Classify this cell by malaria status.
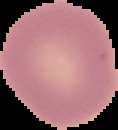

Uninfected.

image size = 118×130 pixels
image type = cell region segmented out of the field of view; surrounding area masked to black
preparation = thin blood smear